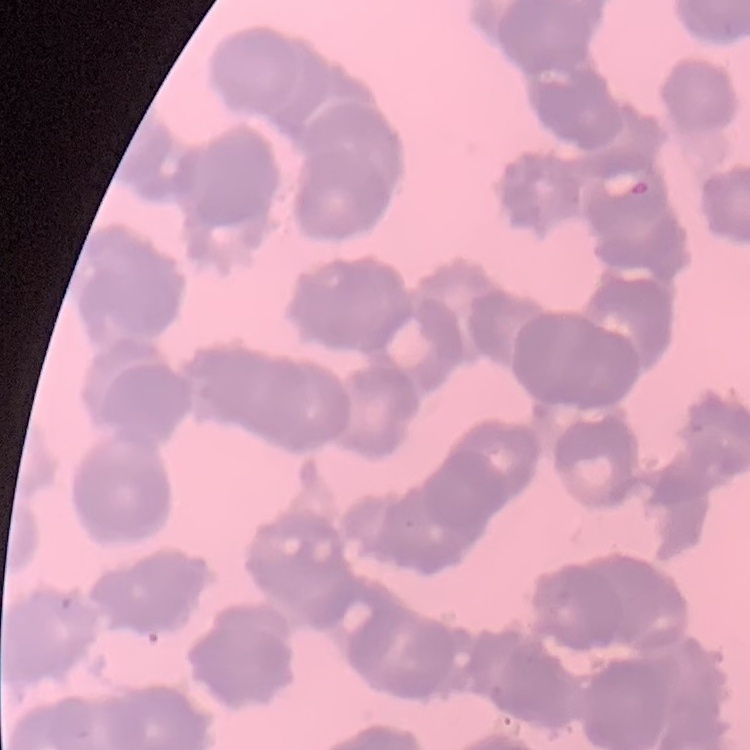

Summary:
  - Red blood cell morphology: rouleaux formation
  - Stain: Field's or Giemsa
  - Preparation: thin blood smear
  - Image type: one tile cut from a larger photomicrograph